Report the malaria status of this cell.
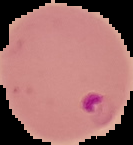

Parasitized.

{
  "preparation": "thin blood film",
  "image_size": "133×145 pixels",
  "image_type": "segmented cell region on a black background"
}